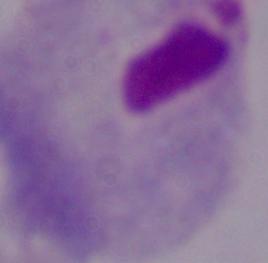

identification: trichomonad
magnification: 1000x
modality: photomicrograph